Locate every Plasmodium falciparum-infected red blood cell.
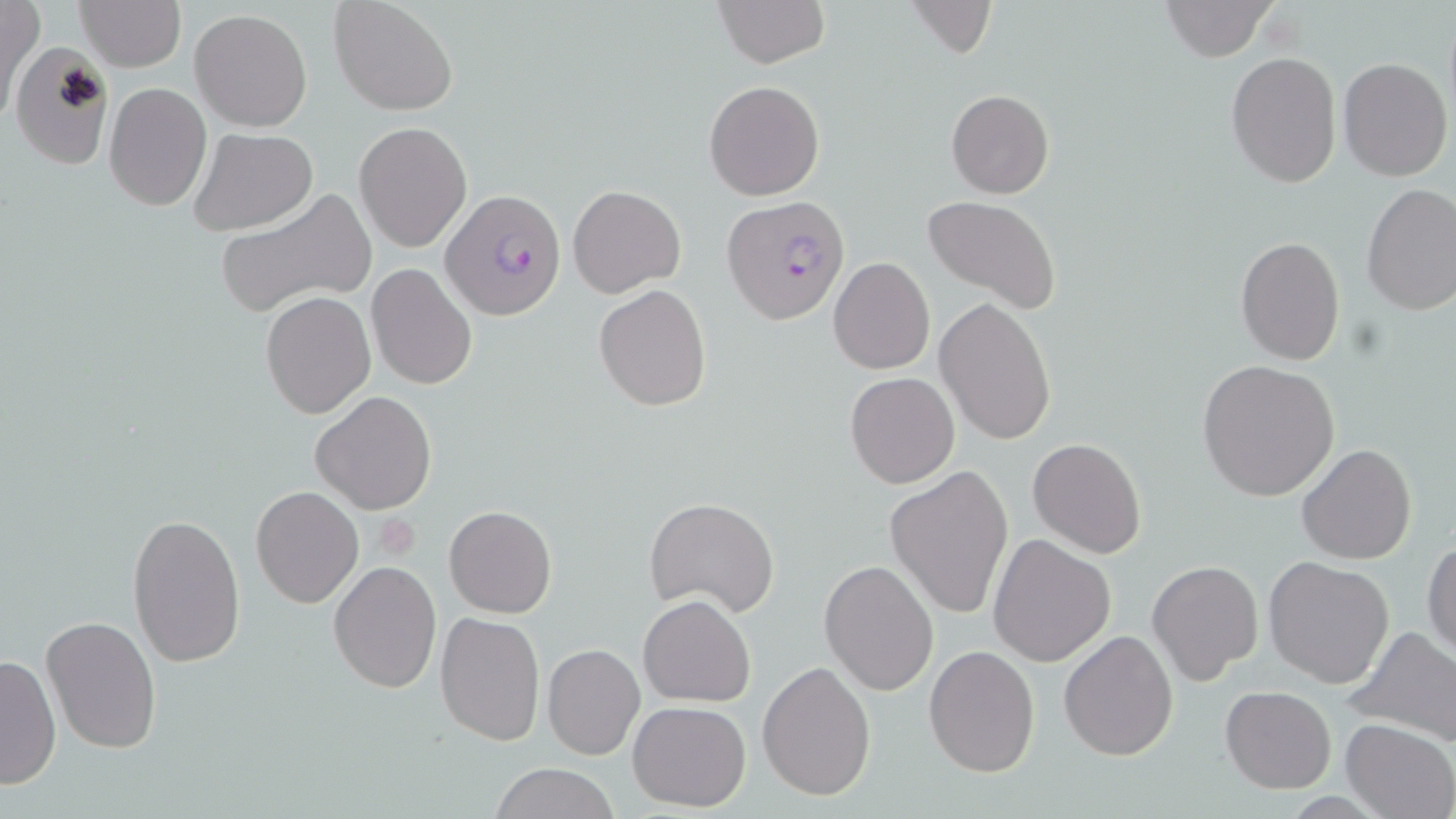
Approximate bounding boxes as (x1,y1)-(x2,y2) corner pairs in pixels.
Plasmodium falciparum-infected red blood cells: (439,188)-(568,322), (723,197)-(849,323).

Uninfected red blood cell locations: (74,0)-(186,71), (328,0)-(458,116), (712,0)-(830,68), (904,0)-(996,58), (1160,0)-(1279,62), (1,1)-(42,122), (189,7)-(313,131), (11,42)-(115,170), (1225,52)-(1343,189), (1337,57)-(1453,182), (704,80)-(823,200), (104,82)-(211,211), (945,89)-(1056,198), (354,122)-(471,253), (187,127)-(317,237), (567,183)-(686,298), (1360,183)-(1456,315), (215,186)-(376,319), (922,196)-(1063,316), (1235,237)-(1344,365), (828,257)-(934,374), (366,262)-(479,391), (594,284)-(711,412), (260,291)-(376,420), (933,297)-(1055,447), (1197,360)-(1339,502), (845,372)-(961,489), (309,391)-(439,515), (1027,437)-(1147,558), (1297,444)-(1416,565), (885,467)-(1014,622), (249,485)-(364,609), (644,497)-(780,618), (444,504)-(557,618), (126,512)-(245,668), (986,534)-(1116,667), (1423,538)-(1455,660), (1263,556)-(1395,688), (819,559)-(939,695), (1147,559)-(1264,686), (328,561)-(441,693), (638,594)-(756,706), (434,612)-(546,747), (40,616)-(163,756), (1346,625)-(1456,748), (1060,630)-(1179,761), (542,644)-(645,762), (924,644)-(1038,776), (0,652)-(60,791), (756,660)-(875,801), (1220,685)-(1337,795), (628,700)-(751,813), (1339,719)-(1455,819), (489,762)-(621,819). Platelet locations: (381,513)-(424,559). Slide-level diagnosis: Plasmodium falciparum. May-Grünwald-Giemsa stain. Single field of view. 1000x magnification. Optical microscopy. Image is 1456×819 pixels. Thin blood film.